Classify this cell by malaria status.
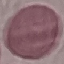

It is uninfected.

Cell patch, automatically extracted from a larger field of view and resized to 64 × 64 pixels. Thin blood smear. Giemsa-stained preparation. Acquired by smartphone through the microscope eyepiece.